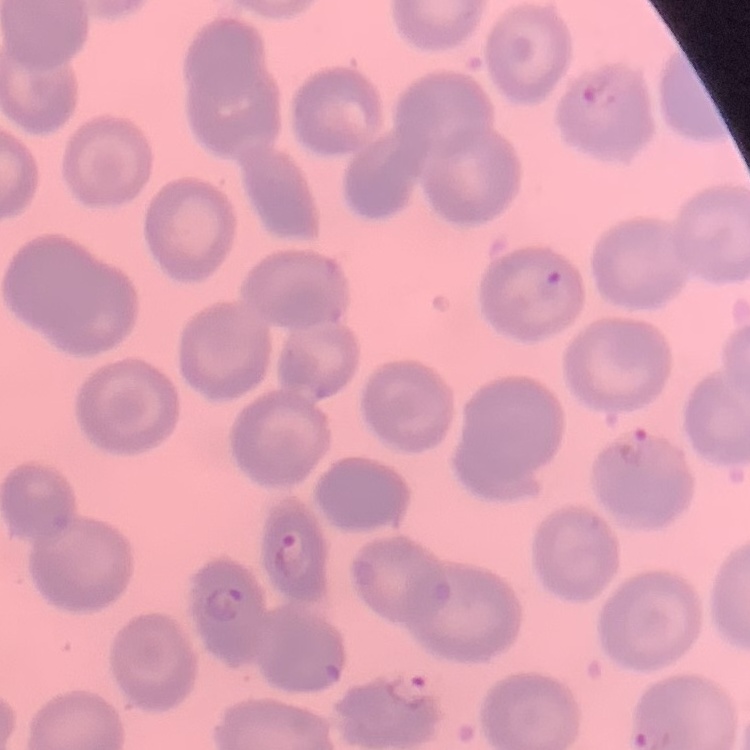
red blood cell morphology = no rouleaux formation
image type = one tile cut from a larger photomicrograph
stain = Field's or Giemsa
preparation = thin blood smear